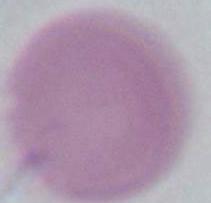

Summary:
  - Identification: red blood cell
  - Modality: micrograph
  - Magnification: 1000x